Locate every blood parasite and identify its species.
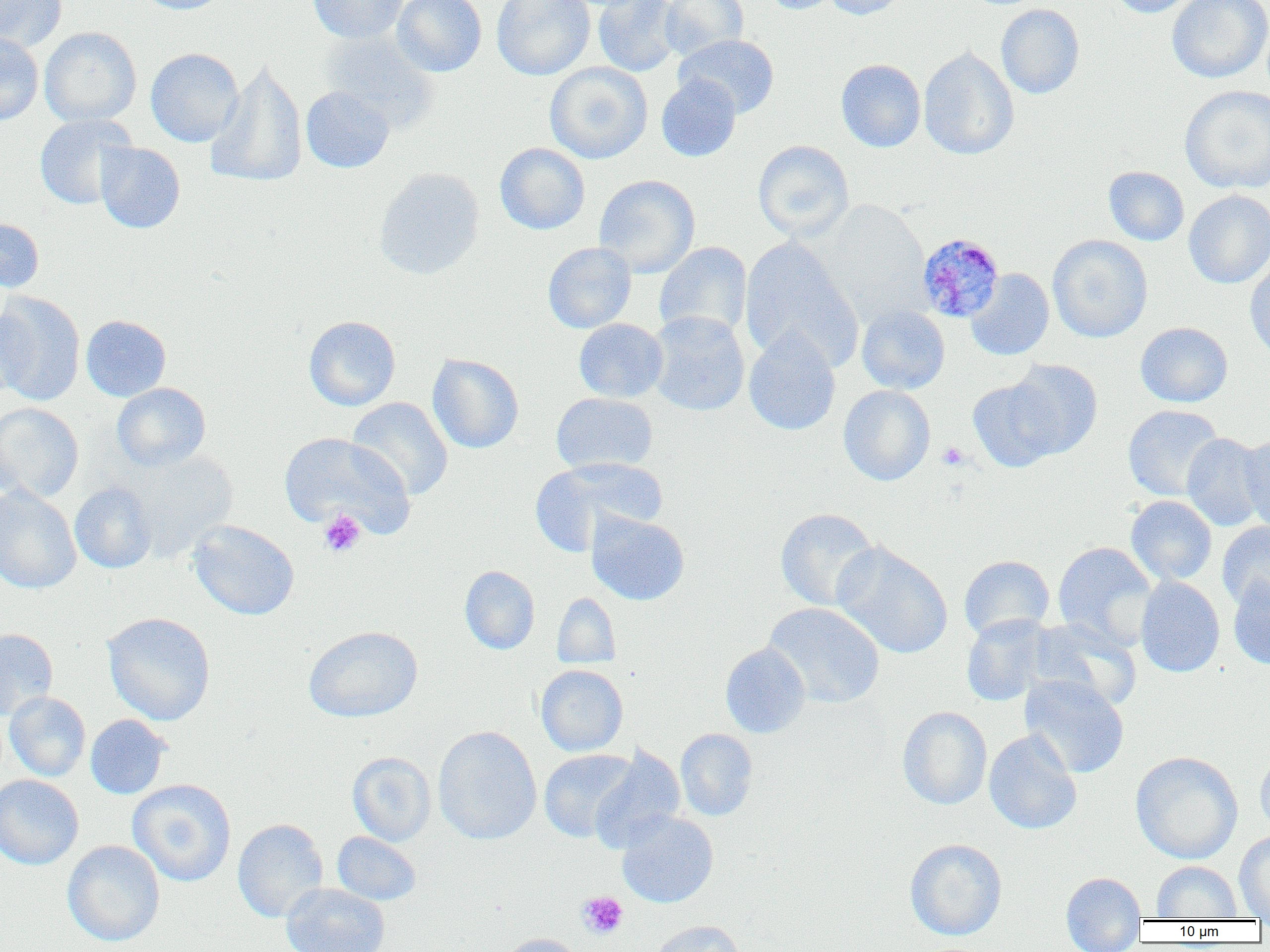

Approximate bounding boxes as (x1, y1, x2, y2) in pixels.
Plasmodium malariae-infected red blood cells: (916, 233, 1005, 323).
No Plasmodium falciparum, Plasmodium ovale, Plasmodium vivax, Babesia divergens, or Trypanosoma brucei observed.

Summary:
  - Platelet locations: (938, 442, 969, 470), (318, 510, 366, 558), (577, 891, 628, 939)
  - Uninfected red blood cell locations: (0, 0, 67, 52), (134, 0, 230, 15), (308, 0, 408, 44), (392, 0, 487, 77), (492, 0, 595, 80), (592, 0, 681, 77), (659, 0, 748, 60), (760, 0, 841, 14), (821, 0, 909, 20), (1106, 0, 1201, 18), (1166, 0, 1270, 83), (996, 3, 1085, 99), (39, 27, 142, 126), (319, 30, 440, 132), (0, 32, 44, 125), (674, 34, 780, 119), (918, 47, 1019, 160), (145, 48, 243, 147), (206, 59, 308, 187), (836, 59, 926, 152), (545, 62, 653, 164), (656, 74, 741, 162), (1179, 85, 1270, 194), (300, 86, 394, 173), (34, 114, 138, 210), (752, 140, 854, 241), (95, 143, 185, 233), (495, 143, 590, 235), (1103, 166, 1189, 246), (373, 167, 485, 280), (594, 175, 700, 278), (1183, 190, 1270, 289), (814, 199, 931, 325), (0, 217, 44, 293), (1047, 234, 1153, 343), (739, 236, 864, 371), (542, 242, 636, 333), (654, 242, 753, 341), (1244, 256, 1270, 363), (965, 268, 1054, 360), (0, 290, 86, 405), (0, 301, 31, 404), (857, 304, 951, 394), (647, 311, 750, 416), (81, 315, 171, 401), (303, 316, 401, 410), (574, 318, 668, 402), (1135, 322, 1233, 407), (744, 329, 841, 435), (427, 353, 524, 453), (1006, 359, 1103, 458), (968, 378, 1064, 472), (112, 383, 211, 471), (838, 384, 936, 486), (551, 392, 659, 475), (346, 397, 453, 500), (0, 402, 84, 502), (1123, 405, 1224, 501), (279, 431, 415, 537), (1181, 433, 1267, 531), (1238, 435, 1270, 534), (119, 450, 238, 563), (530, 456, 667, 555), (69, 482, 158, 574), (0, 484, 81, 594), (1125, 495, 1217, 586), (775, 508, 879, 612), (586, 510, 690, 606), (188, 520, 299, 620), (1217, 522, 1270, 611), (1052, 541, 1158, 652), (832, 542, 953, 659), (958, 555, 1055, 641), (459, 566, 540, 655), (1135, 576, 1224, 677), (1228, 576, 1270, 669), (552, 592, 621, 669), (763, 602, 885, 709), (102, 612, 216, 725), (961, 614, 1055, 706), (1028, 619, 1141, 711), (303, 625, 423, 722), (0, 627, 58, 721), (720, 642, 811, 738), (536, 664, 628, 756), (1020, 675, 1129, 778), (5, 691, 91, 781), (5, 703, 171, 788), (897, 706, 992, 809), (85, 714, 171, 799), (432, 726, 542, 845), (675, 728, 759, 820), (984, 729, 1081, 834), (590, 746, 685, 853), (539, 749, 640, 843), (1255, 750, 1270, 839), (347, 751, 436, 846), (1130, 751, 1243, 864), (0, 774, 84, 870), (127, 779, 236, 887), (617, 811, 718, 908), (232, 819, 329, 922), (332, 831, 421, 906), (1234, 831, 1270, 918), (62, 839, 165, 946), (905, 839, 1007, 940), (1152, 860, 1243, 920), (1061, 872, 1147, 951), (281, 882, 389, 952), (648, 920, 745, 952), (497, 933, 585, 952)
  - Slide-level diagnosis: Plasmodium malariae
  - Magnification: 1000x
  - Preparation: thin blood smear
  - Field of view: one of a larger specimen
  - Modality: optical microscopy
  - Image size: 1270×952 pixels